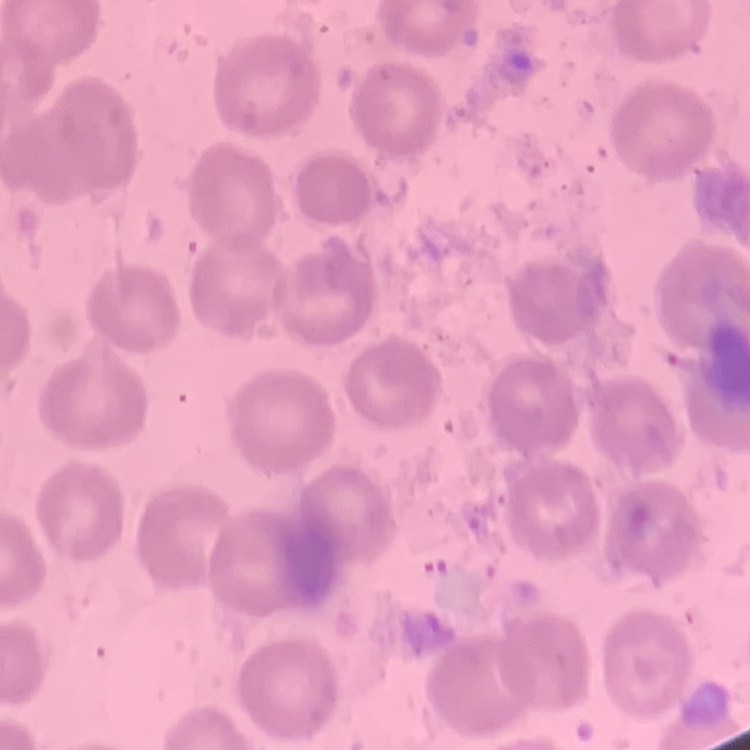
Summary:
  - Erythrocyte morphology: no rouleaux formation
  - Stain: Field's or Giemsa
  - Image type: one tile cut from a larger photomicrograph
  - Preparation: thin blood film